Give the extent of all uninfected red blood cells.
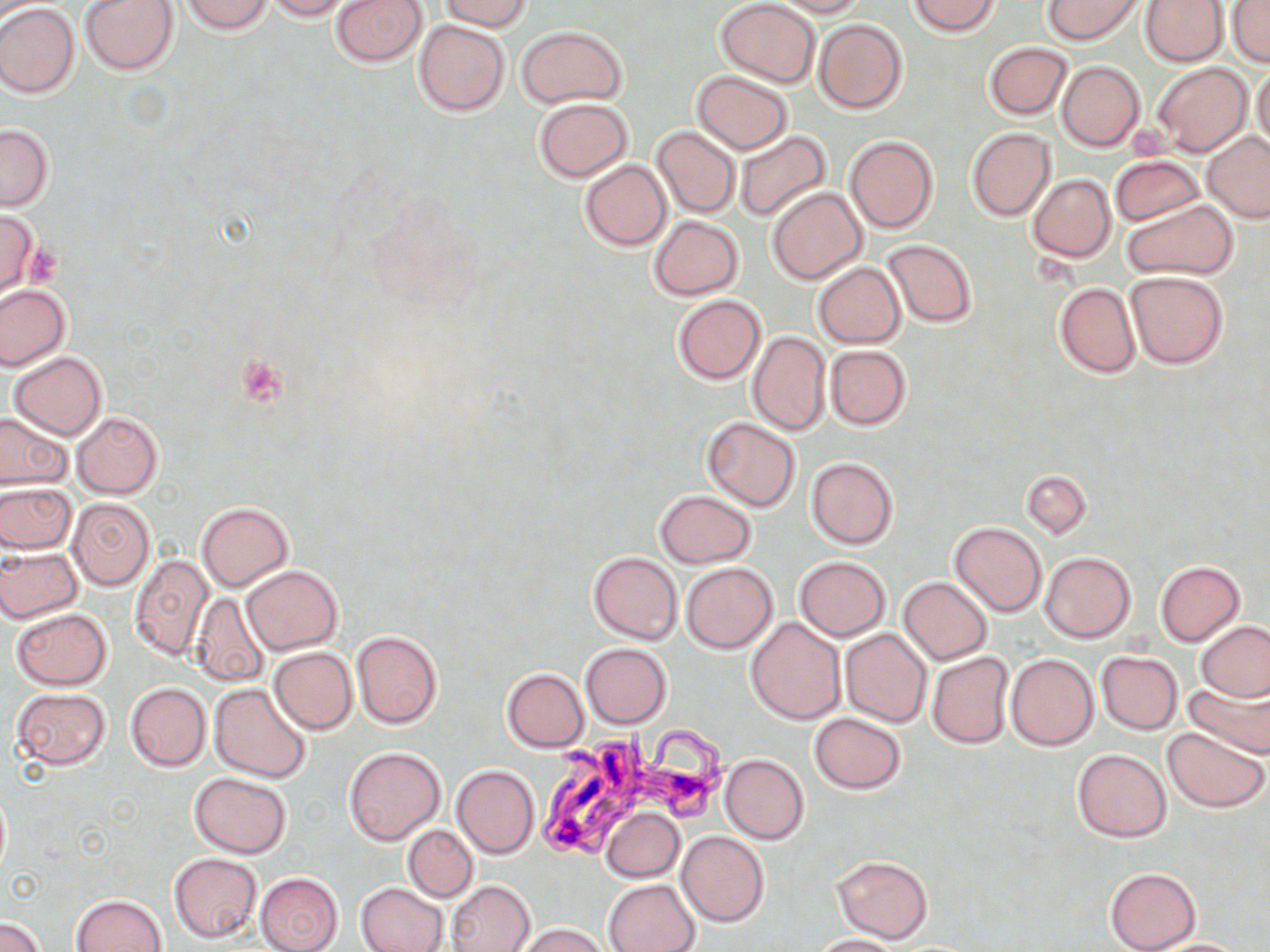
Approximate bounding boxes as (x1, y1, x2, y2) in pixels.
Uninfected red blood cells: (81, 0, 178, 75), (182, 0, 273, 36), (263, 0, 353, 21), (330, 0, 427, 68), (437, 0, 532, 32), (715, 0, 821, 88), (768, 0, 869, 17), (908, 0, 1002, 37), (1041, 0, 1147, 45), (1140, 0, 1227, 67), (1229, 2, 1270, 68), (0, 4, 79, 98), (813, 18, 909, 116), (414, 19, 511, 117), (515, 24, 628, 108), (982, 43, 1072, 120), (1057, 60, 1146, 152), (1151, 62, 1252, 156), (1251, 64, 1270, 152), (690, 71, 794, 154), (532, 98, 633, 181), (0, 124, 54, 211), (651, 125, 741, 219), (966, 127, 1056, 221), (734, 130, 834, 223), (1202, 131, 1270, 223), (846, 136, 940, 234), (1110, 155, 1203, 226), (578, 159, 671, 251), (1027, 174, 1116, 262), (767, 186, 868, 284), (1122, 199, 1239, 281), (0, 210, 41, 296), (647, 216, 745, 300), (879, 239, 979, 327), (814, 263, 906, 348), (1124, 270, 1229, 369), (1055, 283, 1140, 378), (0, 284, 70, 371), (671, 294, 767, 385), (746, 331, 831, 437), (825, 345, 911, 429), (8, 351, 108, 439), (0, 409, 72, 491), (71, 412, 163, 499), (701, 417, 801, 511), (805, 457, 898, 550), (1021, 470, 1092, 539), (0, 482, 75, 554), (654, 489, 757, 568), (66, 497, 155, 590), (196, 501, 293, 593), (949, 522, 1047, 616), (0, 546, 83, 623), (1039, 551, 1136, 642), (588, 552, 682, 644), (127, 554, 214, 661), (794, 556, 891, 642), (1154, 560, 1246, 645), (680, 561, 778, 654), (241, 564, 343, 655), (898, 577, 994, 664), (189, 593, 269, 686), (11, 607, 112, 690), (747, 616, 846, 724), (1196, 620, 1270, 703), (840, 628, 931, 728), (351, 630, 443, 729), (581, 643, 673, 729), (268, 647, 358, 735), (1096, 651, 1183, 735), (926, 652, 1014, 748), (1006, 653, 1098, 751), (501, 668, 589, 752), (1183, 676, 1270, 757), (125, 682, 210, 771), (210, 683, 313, 785), (9, 688, 110, 771), (809, 712, 907, 794), (1162, 726, 1269, 813), (344, 746, 445, 845), (1073, 749, 1171, 841), (721, 753, 809, 844), (452, 765, 540, 859), (189, 772, 293, 857), (602, 807, 684, 882), (402, 824, 479, 902), (676, 830, 770, 926), (168, 852, 263, 944), (832, 855, 934, 944), (1103, 866, 1202, 952), (255, 872, 344, 952), (603, 879, 700, 952), (446, 880, 536, 952), (355, 883, 448, 952), (70, 893, 170, 952), (1, 915, 47, 952), (513, 923, 613, 952), (812, 933, 906, 952), (1140, 938, 1258, 951).

slide_level_diagnosis: Trypanosoma brucei
field_of_view: one of a larger specimen
magnification: 1000x
trypanosoma_brucei_locations: 'approximate bounding boxes as (x1, y1, x2, y2) in pixels: (531, 722, 735, 860)'
preparation: thin blood film
platelet_locations: 'approximate bounding boxes as (x1, y1, x2, y2) in pixels: (22, 243, 63, 288), (237, 355, 287, 407)'
stain: May-Grünwald-Giemsa
modality: optical microscopy
image_size: 1270×952 pixels